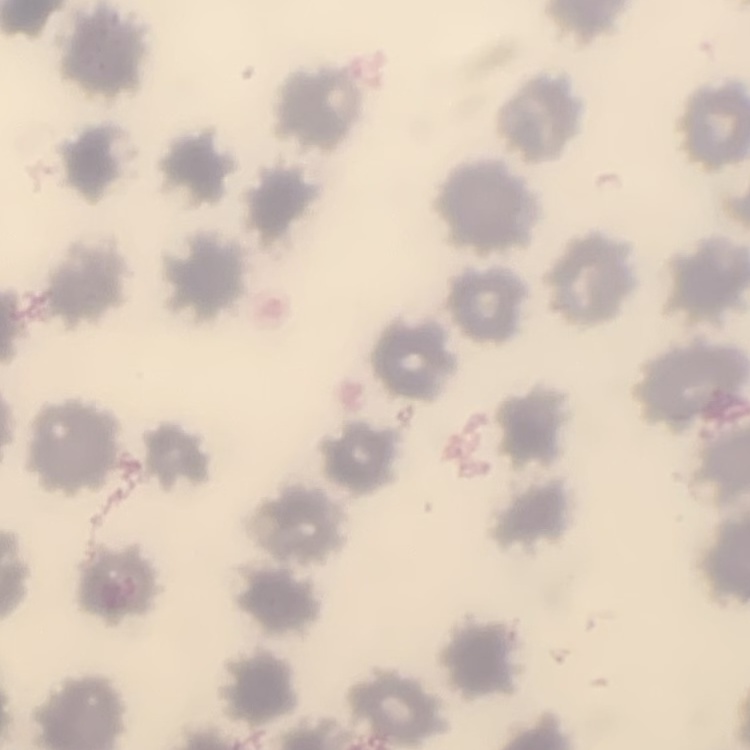

erythrocyte morphology = no rouleaux formation
stain = Field's or Giemsa
preparation = thin blood smear
image type = square crop of a larger photomicrograph